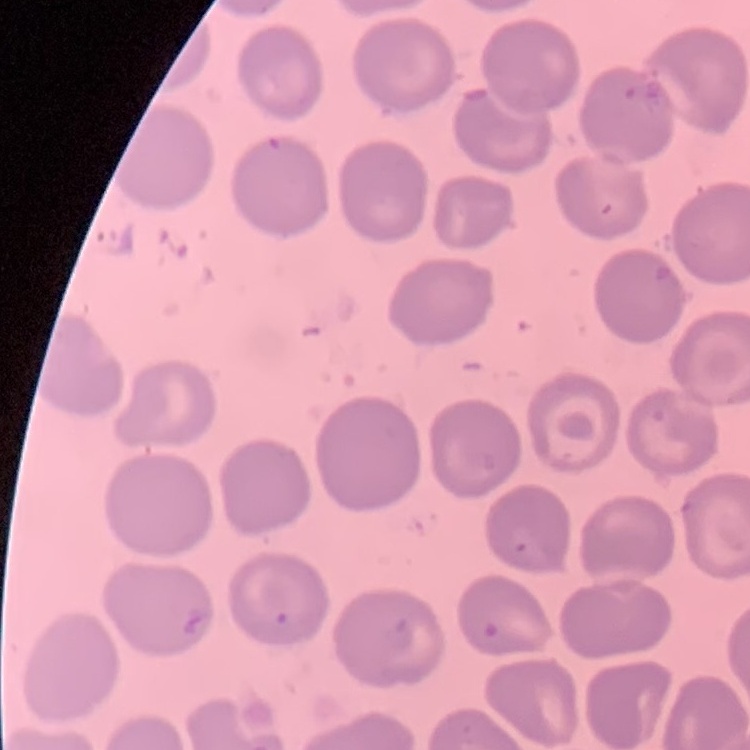 The erythrocytes exhibit no rouleaux formation. One tile cut from a larger photomicrograph. Field's or Giemsa stain. Thin blood smear.